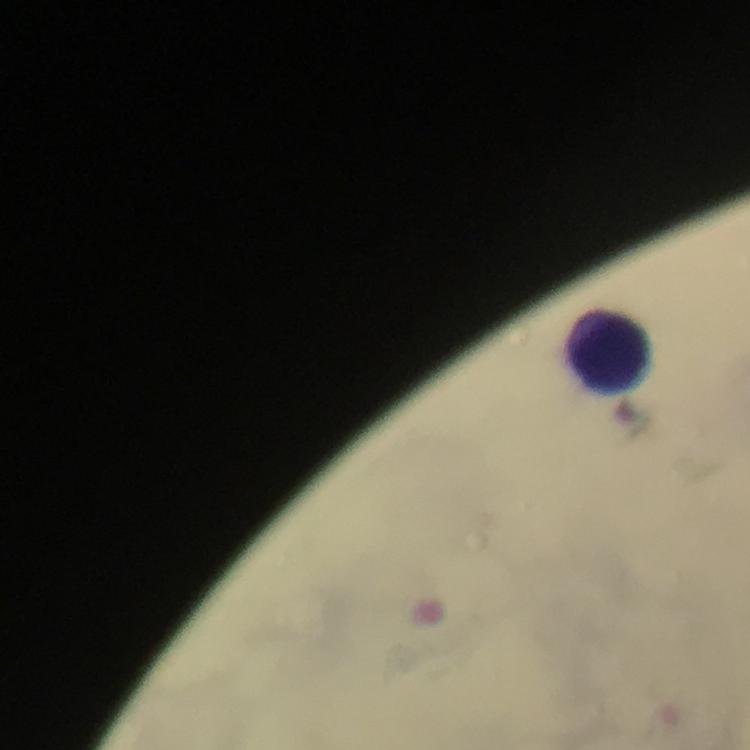
Approximate centers as (x, y) in pixels. Leukocyte locations: (609, 350). From a malaria diagnostic workup. Smartphone photograph taken through a microscope. Image is 750×750 pixels. A crop from one field of view. Plasmodium parasites: none seen. Immersion oil was used. Giemsa-stained preparation. 100x magnification. Thick blood film.